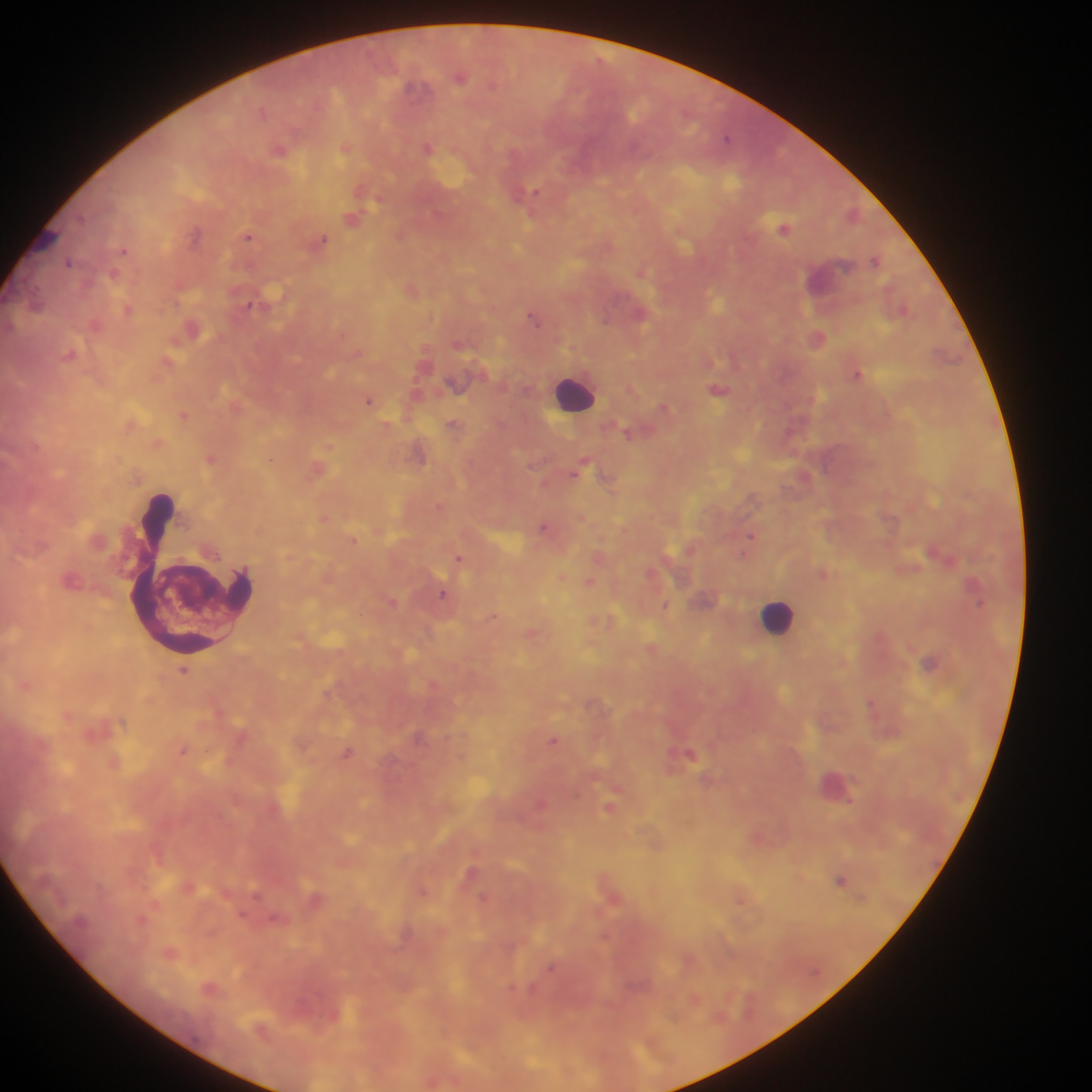
{
  "country": "Ghana",
  "leukocyte_locations": "approximate centers as (x, y) in pixels: (573, 393), (192, 570), (778, 616)",
  "plasmodium_parasite_locations": "approximate centers as (x, y) in pixels: (460, 77), (413, 87), (262, 111), (727, 138), (428, 148), (278, 150), (344, 151), (535, 191), (352, 220), (785, 228), (195, 234), (248, 236), (321, 240), (123, 250), (875, 260), (69, 261), (641, 272), (128, 309), (535, 319), (818, 338), (858, 374), (719, 390), (368, 400), (183, 415), (452, 424), (789, 431), (627, 433), (211, 459), (271, 459), (580, 468), (543, 526), (750, 537), (353, 541), (746, 548), (458, 557), (589, 582), (971, 585), (443, 593), (392, 603), (979, 604), (665, 606), (492, 616), (930, 662), (184, 671), (872, 704), (553, 739), (183, 751), (347, 754), (691, 754), (609, 808), (840, 880), (483, 897), (551, 968)",
  "preparation": "thick blood film",
  "field_of_view": "single",
  "image_size": "1092×1092 pixels",
  "capture": "mobile-phone photograph through a microscope"
}